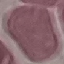
{
  "result": "no malaria parasites seen",
  "preparation": "thin smear",
  "stain": "Giemsa",
  "capture": "smartphone through the microscope eyepiece",
  "image_type": "cell patch, automatically extracted from a larger field of view and resized to 64 × 64 pixels"
}